Identify the preparation type.
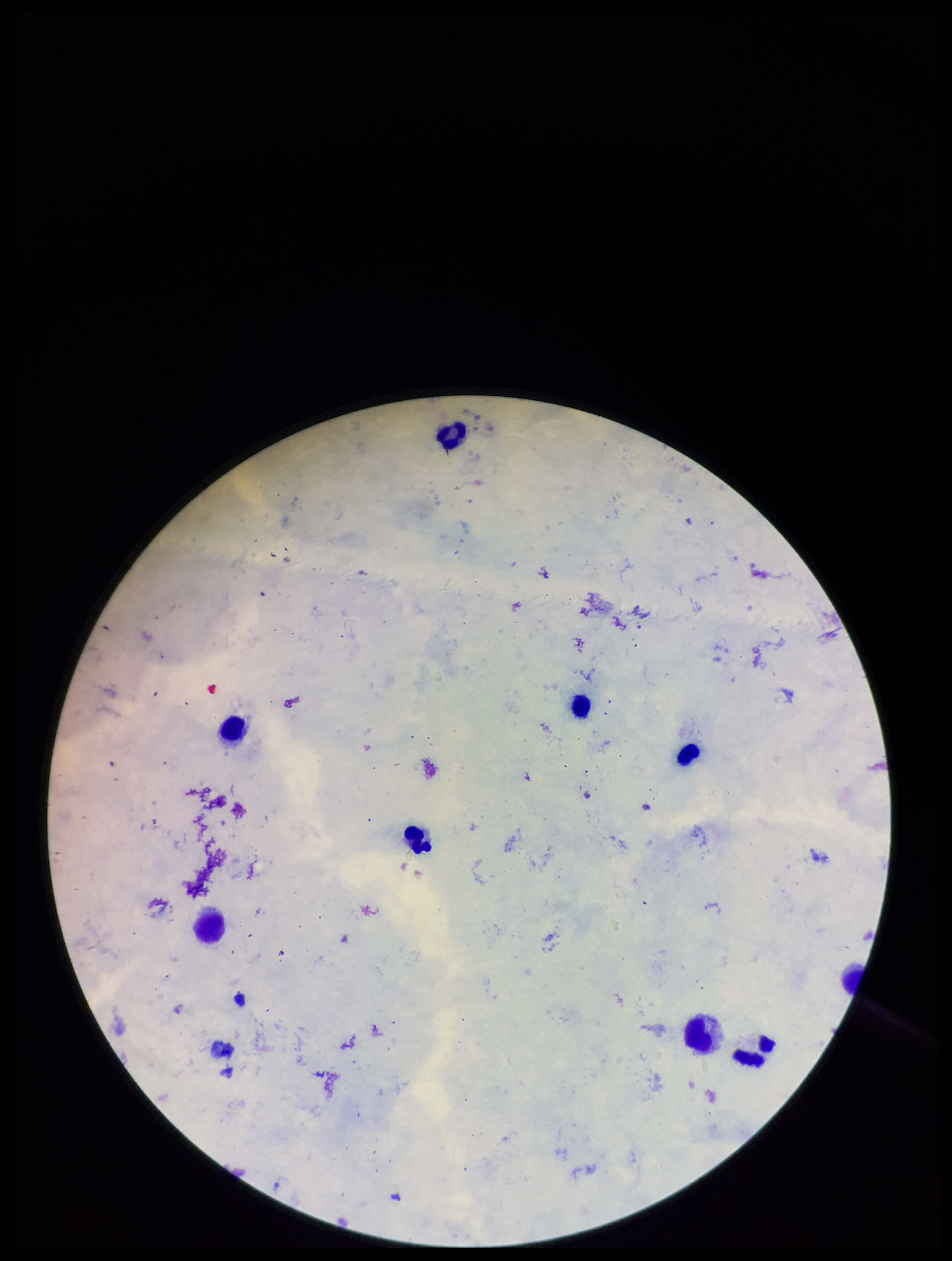

Thick.

capture: smartphone photograph through the microscope eyepiece
parasite_count: 0
field_of_view: single
species_reported_for_this_patient: Plasmodium falciparum
patient_malaria_status: positive
plasmodium_parasites: none seen
leukocyte_count: 8
stain: Giemsa
image_size: 952×1261 pixels